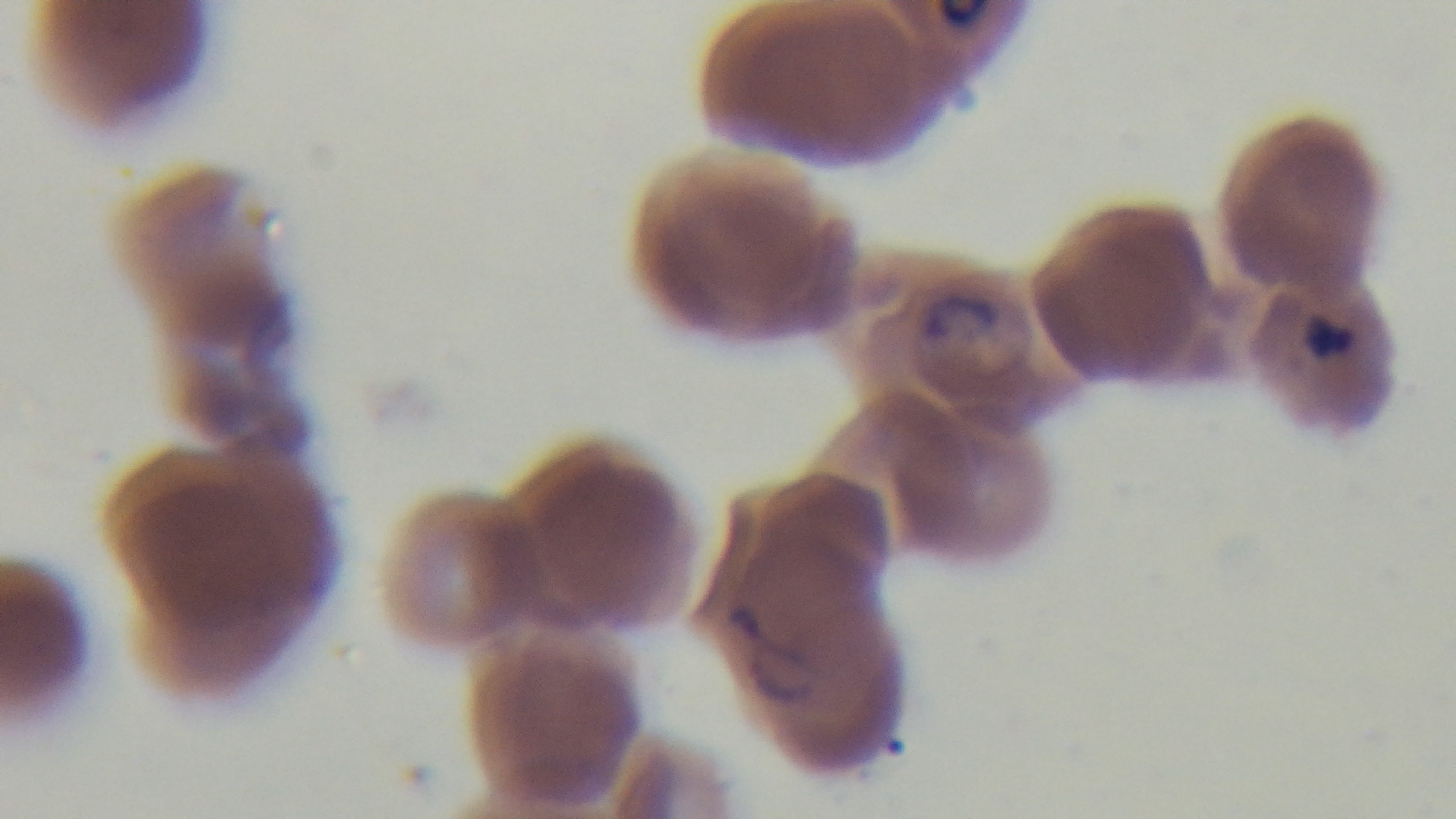
Summary:
  - Field of view: one from the slide
  - Capture: mounted 4K digital camera
  - Objective: 100x oil immersion
  - Stain: Giemsa
  - Malaria status: infected
  - Preparation: thin blood film
  - Modality: light microscopy